Assess the morphology of the erythrocytes.
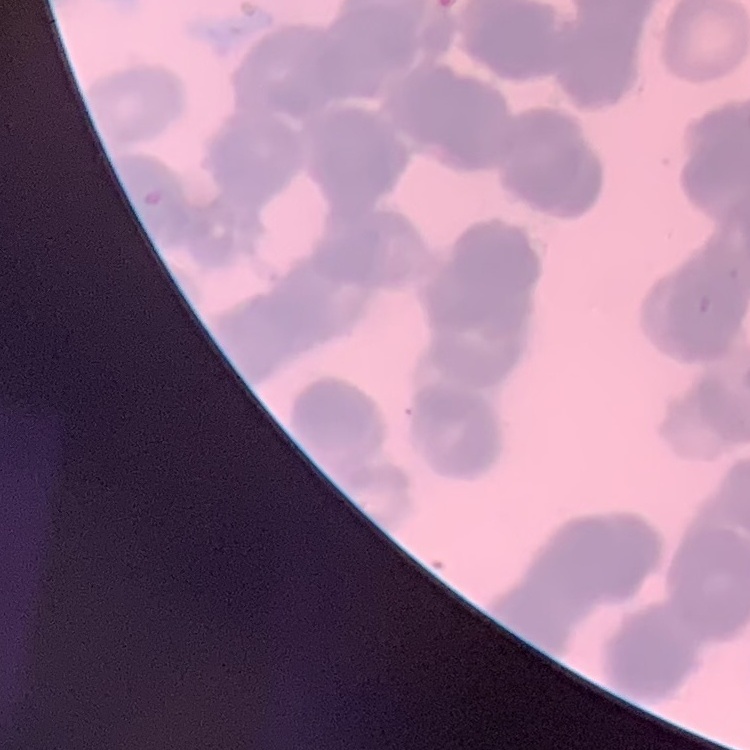
They show rouleaux formation.

Stained with either Field's or Giemsa. Thin peripheral smear. Square crop of a larger photomicrograph.